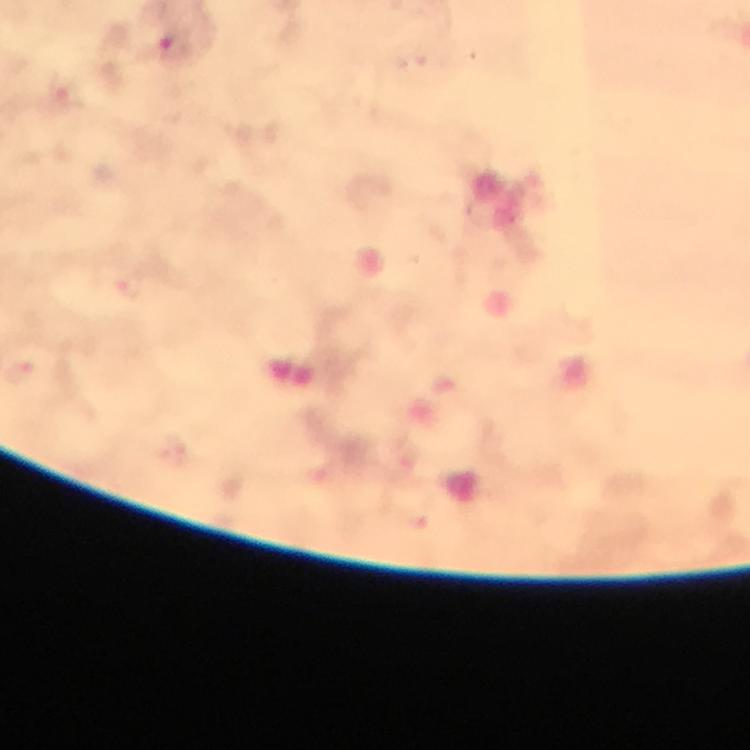

{
  "magnification": "100x",
  "malaria_parasite_locations": "approximate centers as {x, y} in pixels: {174, 48}",
  "context": "from a diagnostic examination for malaria",
  "stain": "Giemsa",
  "preparation": "thick smear",
  "cropped_from": "one field of view",
  "image_size": "750×750 pixels",
  "immersion_oil": "used",
  "capture": "smartphone camera through the microscope"
}